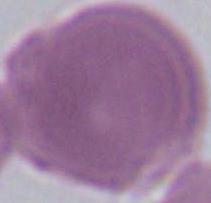

identification = erythrocyte
modality = micrograph
magnification = 1000x